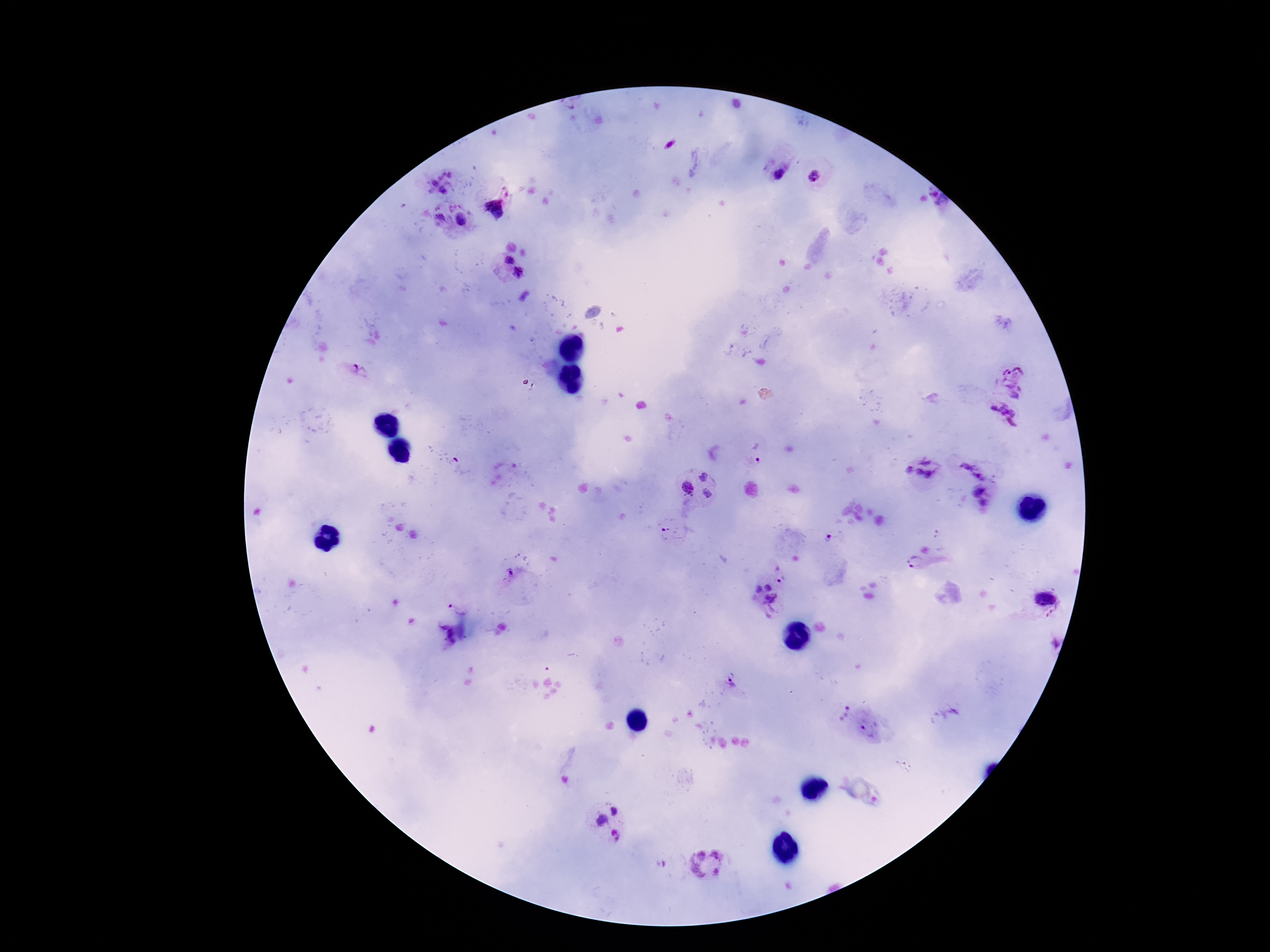
patient_malaria_status: infected
magnification: 100x
preparation: thick blood film
plasmodium_parasite_locations: 'approximate centers as [x, y] in pixels: [670, 144], [441, 175], [451, 175], [778, 175], [815, 177], [434, 183], [443, 190], [935, 194], [943, 201], [496, 209], [440, 217], [461, 218], [508, 260], [518, 273], [358, 370], [1015, 382], [1001, 422], [758, 459], [455, 460], [925, 461], [979, 467], [909, 469], [918, 472], [928, 474], [704, 476], [688, 488], [976, 491], [707, 493], [982, 503], [831, 536], [915, 562], [780, 572], [511, 573], [767, 587], [758, 588], [1045, 598], [772, 605], [732, 683], [844, 713], [869, 730], [615, 811], [601, 821], [616, 836], [707, 865]'
capture: smartphone camera through the microscope eyepiece
field_of_view: single
stain: Giemsa
image_size: 1270×952 pixels